Classify this cell by malaria status.
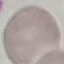

It is uninfected.

{
  "preparation": "thin smear",
  "capture": "smartphone through the microscope eyepiece",
  "image_type": "automatically extracted cell patch, resized to 64 × 64 pixels",
  "stain": "Giemsa"
}